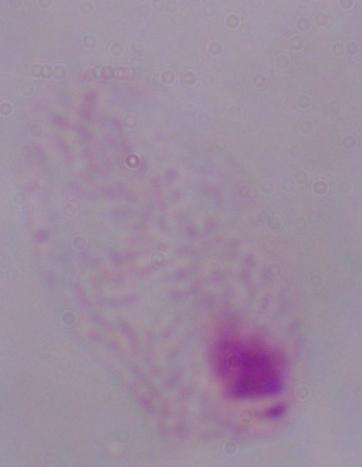 Photomicrograph. A trichomonad is shown. 1000x magnification.